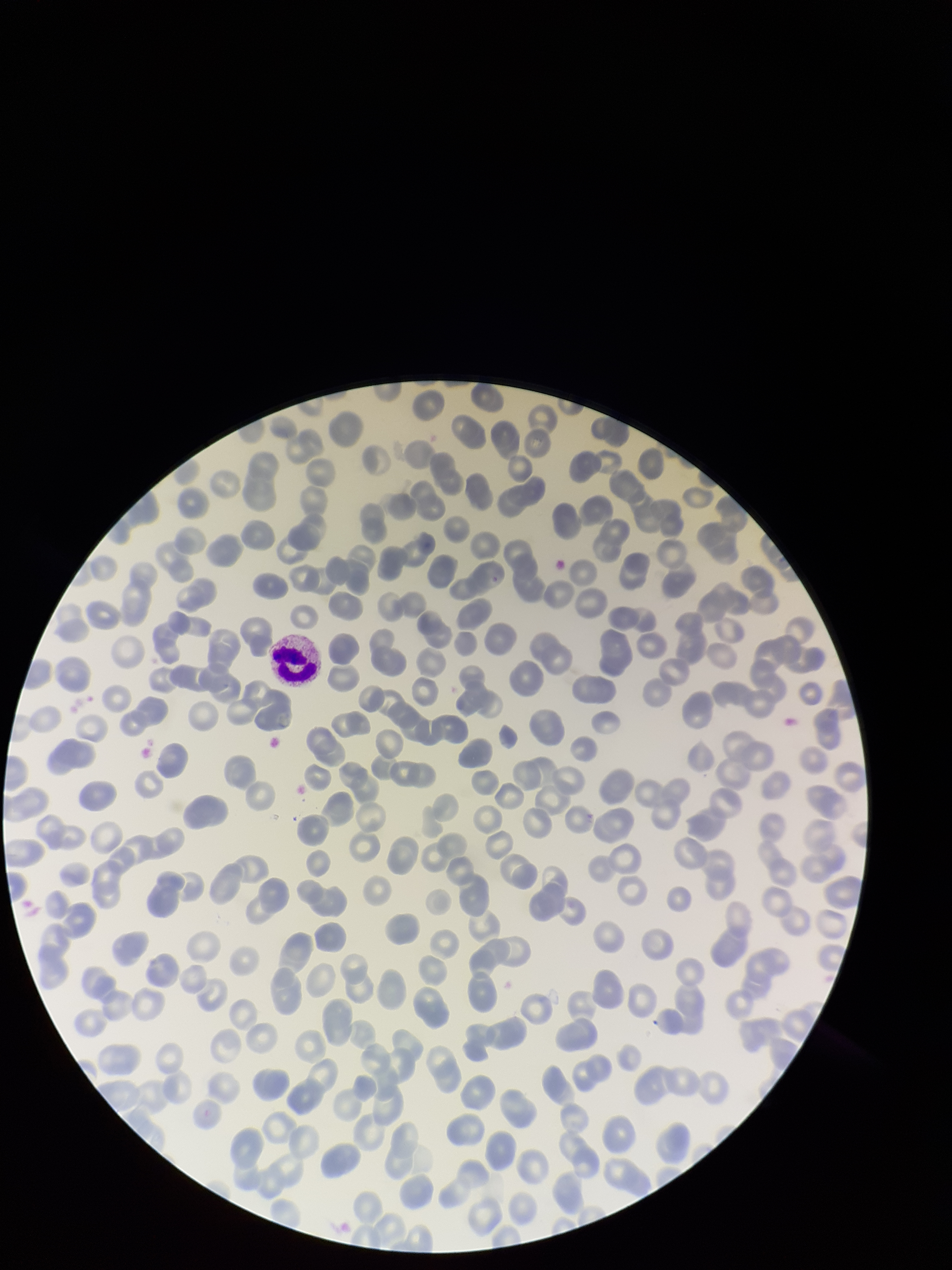

Summary:
  - Parasitized red blood cells: none detected
  - Image size: 952×1270 pixels
  - Patient malaria status: positive
  - Capture: smartphone photograph through the microscope eyepiece
  - Stain: Giemsa
  - Preparation: thin
  - Field of view: single
  - Red blood cell count: 255
  - Species reported for this patient: Plasmodium falciparum
  - Parasitized red blood cell count: 0